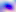
400x magnification. Photomicrograph. Toxoplasma gondii is seen.